Classify this cell by malaria status.
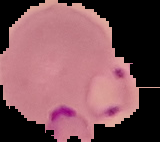

Parasitized.

From a thin blood smear. Segmented cell region on a black background. Image is 160×142 pixels.